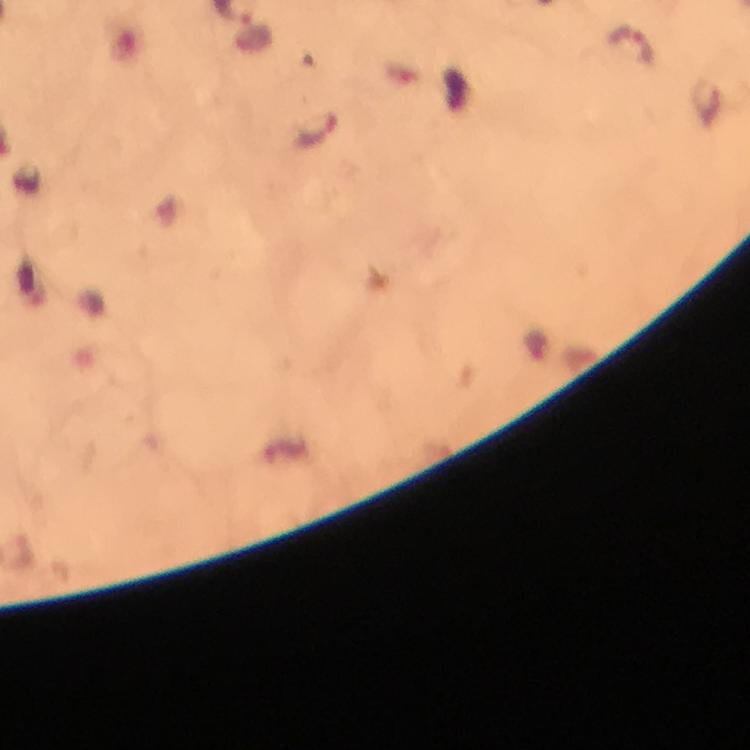

Approximate centers as {x, y} in pixels.
Summary:
  - Plasmodium parasite locations: {633, 47}, {320, 132}
  - Preparation: thick blood film
  - Image size: 750×750 pixels
  - Context: from a malaria diagnostic workup
  - Stain: Giemsa
  - Cropped from: a single field of view
  - Immersion oil: applied
  - Magnification: 100x
  - Capture: smartphone photograph through a microscope